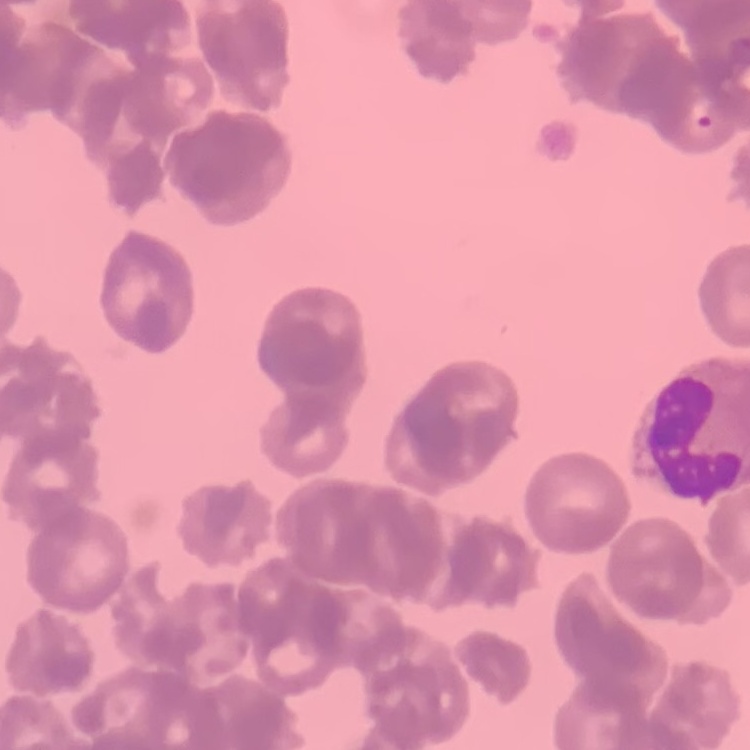

The red blood cells exhibit rouleaux formation. Thin peripheral smear. Field's or Giemsa stain. Square crop of a larger photomicrograph.